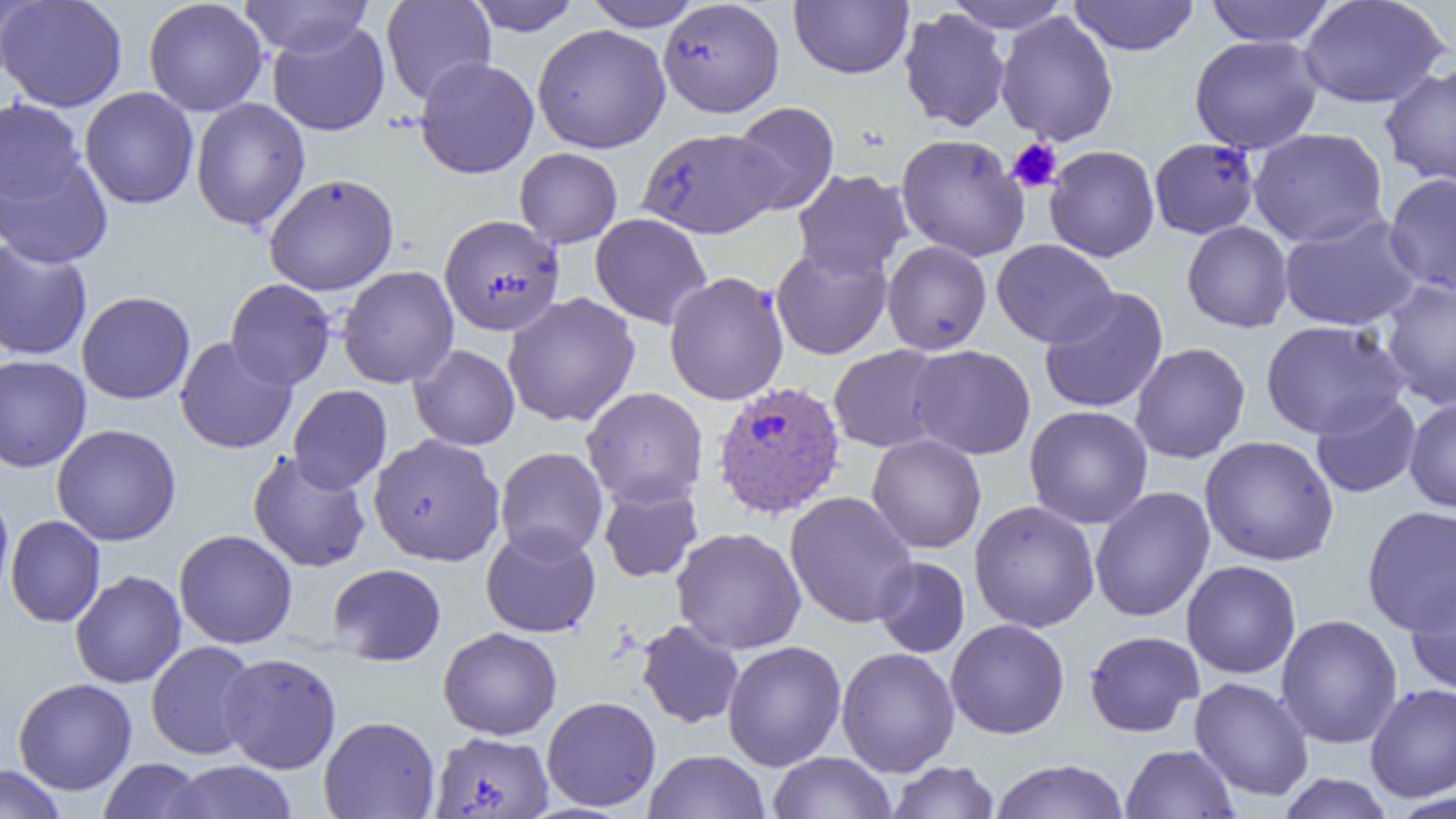
Summary:
  - Coordinate format: approximate bounding boxes as [x1, y1, x2, y2] in pixels
  - Plasmodium vivax-infected red blood cell locations: [713, 381, 847, 520]
  - Platelet locations: [1006, 137, 1062, 193]
  - Uninfected red blood cell locations: [0, 0, 43, 82], [1, 0, 127, 112], [143, 0, 268, 116], [238, 0, 374, 57], [466, 0, 582, 35], [582, 0, 704, 31], [789, 0, 913, 78], [943, 0, 1072, 34], [1068, 0, 1200, 55], [1204, 0, 1338, 46], [1297, 0, 1450, 109], [381, 1, 496, 105], [660, 2, 785, 118], [899, 7, 1010, 132], [996, 12, 1118, 146], [267, 21, 390, 136], [533, 24, 671, 153], [1189, 34, 1323, 154], [416, 45, 670, 163], [415, 56, 539, 179], [1380, 64, 1456, 188], [80, 87, 199, 209], [191, 97, 310, 231], [0, 98, 88, 210], [730, 102, 839, 214], [1249, 127, 1388, 247], [635, 129, 780, 239], [896, 133, 1030, 261], [1149, 137, 1260, 239], [0, 143, 113, 269], [1044, 145, 1160, 261], [514, 147, 622, 247], [791, 168, 913, 281], [264, 173, 399, 295], [1384, 173, 1456, 296], [1278, 212, 1423, 331], [590, 213, 712, 329], [439, 216, 564, 336], [1182, 221, 1293, 332], [0, 238, 93, 360], [991, 239, 1118, 348], [882, 241, 992, 355], [771, 243, 892, 360], [338, 266, 459, 389], [664, 272, 789, 406], [1379, 277, 1456, 410], [225, 278, 336, 390], [1038, 287, 1168, 413], [77, 291, 195, 404], [502, 293, 640, 427], [1260, 319, 1408, 438], [175, 337, 297, 454], [1130, 342, 1250, 463], [409, 345, 520, 450], [828, 345, 950, 453], [908, 345, 1036, 459], [0, 354, 91, 472], [288, 385, 392, 494], [581, 387, 708, 508], [1310, 392, 1421, 499], [1405, 395, 1456, 513], [1024, 405, 1153, 528], [52, 424, 182, 546], [368, 433, 505, 566], [867, 434, 986, 553], [1200, 435, 1339, 565], [495, 447, 608, 563], [248, 451, 371, 572], [599, 483, 702, 582], [1089, 486, 1215, 622], [0, 487, 14, 608], [785, 491, 918, 628], [969, 500, 1100, 632], [1362, 505, 1456, 635], [5, 515, 105, 627], [481, 526, 601, 638], [671, 527, 806, 654], [174, 529, 297, 649], [872, 557, 969, 657], [1182, 560, 1301, 679], [328, 563, 446, 665], [70, 570, 186, 688], [1406, 578, 1456, 697], [1276, 614, 1403, 749], [945, 619, 1070, 739], [636, 621, 744, 729], [438, 627, 562, 739], [1084, 630, 1204, 737], [146, 641, 260, 760], [722, 641, 846, 771], [836, 647, 959, 777], [218, 652, 342, 773], [1189, 677, 1314, 801], [13, 678, 137, 795], [1365, 683, 1456, 802], [542, 696, 661, 812], [319, 716, 440, 819], [428, 734, 551, 819], [1121, 744, 1239, 819], [644, 750, 770, 819], [768, 751, 896, 819], [98, 758, 206, 818], [988, 759, 1130, 818], [161, 760, 299, 819], [886, 761, 1000, 819], [0, 765, 67, 819], [1276, 774, 1396, 818]
  - Slide-level diagnosis: Plasmodium vivax
  - Modality: light microscopy
  - Field of view: one of a larger specimen
  - Magnification: 1000x
  - Image size: 1456×819 pixels
  - Preparation: thin blood film